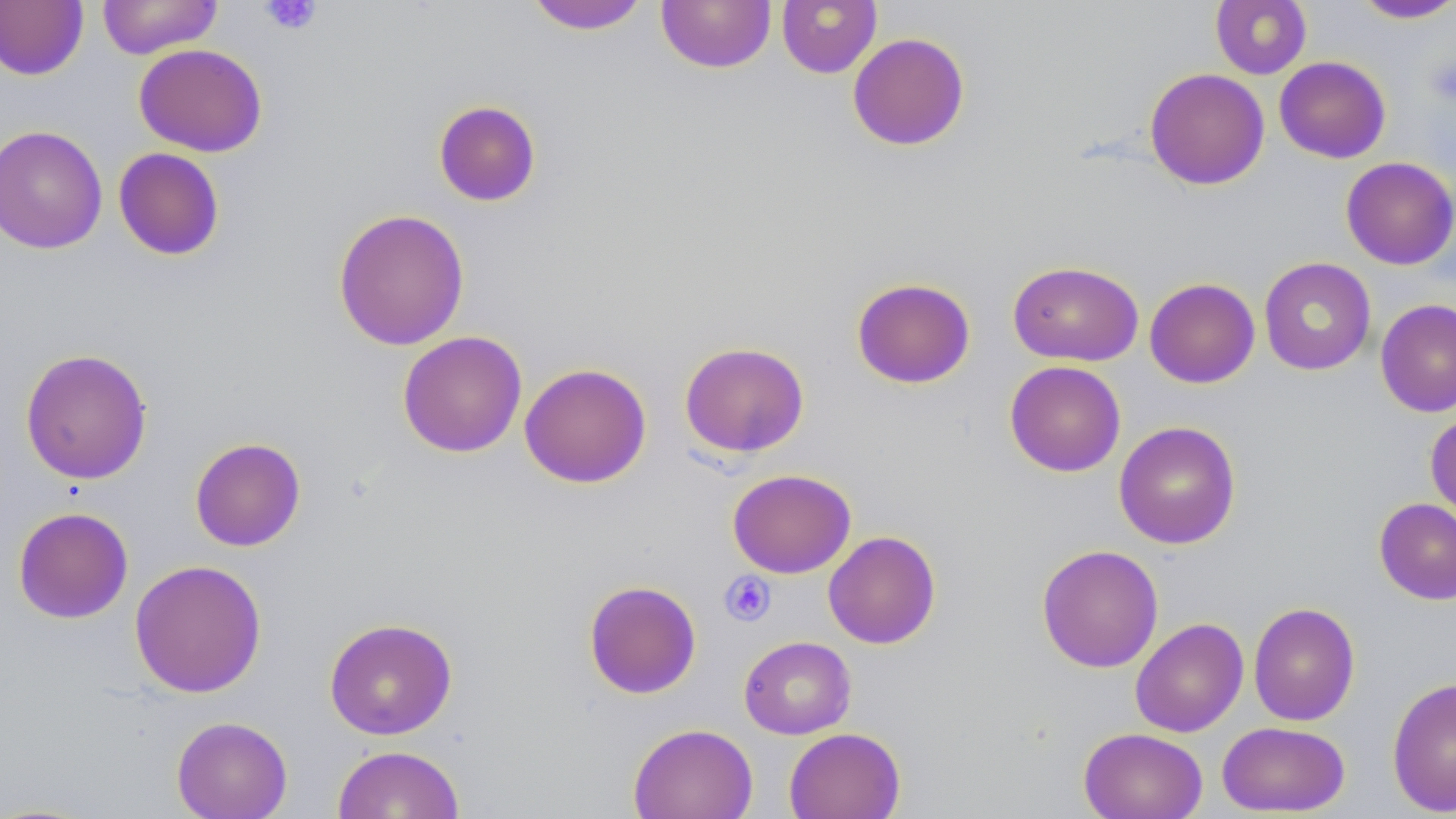

Summary:
  - Coordinate format: approximate bounding boxes as [x1, y1, x2, y2] in pixels
  - Uninfected red blood cell locations: [97, 0, 222, 59], [656, 0, 776, 73], [776, 0, 882, 78], [1210, 0, 1312, 79], [1351, 0, 1456, 24], [0, 1, 89, 81], [525, 1, 650, 34], [847, 31, 970, 151], [133, 43, 268, 157], [1274, 56, 1391, 163], [1144, 68, 1270, 190], [433, 99, 542, 207], [0, 124, 108, 254], [113, 147, 225, 261], [1340, 156, 1456, 270], [332, 208, 470, 351], [1258, 257, 1377, 375], [1007, 260, 1143, 366], [851, 277, 976, 389], [1144, 277, 1260, 388], [1375, 299, 1456, 418], [397, 330, 527, 458], [678, 341, 810, 458], [19, 348, 153, 485], [1004, 360, 1126, 477], [518, 362, 652, 488], [1425, 412, 1456, 524], [1114, 420, 1241, 549], [189, 437, 306, 551], [727, 468, 857, 578], [1374, 497, 1456, 605], [12, 506, 134, 624], [823, 530, 942, 649], [1036, 544, 1164, 673], [129, 559, 267, 698], [583, 579, 702, 699], [1248, 602, 1361, 726], [323, 617, 458, 740], [1130, 617, 1249, 737], [738, 635, 856, 739], [1387, 676, 1456, 816], [170, 715, 293, 819], [1217, 721, 1351, 816], [628, 722, 758, 819], [783, 727, 906, 819], [1078, 727, 1208, 819], [332, 744, 465, 819]
  - Platelet locations: [259, 0, 322, 36], [1425, 57, 1456, 106], [720, 571, 776, 626]
  - Slide-level diagnosis: no evidence of blood parasites
  - Preparation: thin blood smear
  - Image size: 1456×819 pixels
  - Field of view: single
  - Modality: light microscopy
  - Magnification: 1000x
  - Stain: May-Grünwald-Giemsa